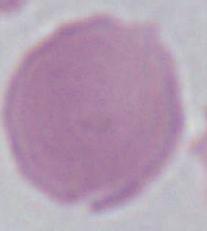
identification = red blood cell
magnification = 1000x
modality = photomicrograph